Assess this cell for malaria.
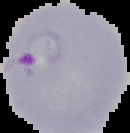
It is parasitized.

image_size: 130×133 pixels
image_type: segmented cell region with the area outside set to black
preparation: thin blood film